Comment on the morphology of the red blood cells.
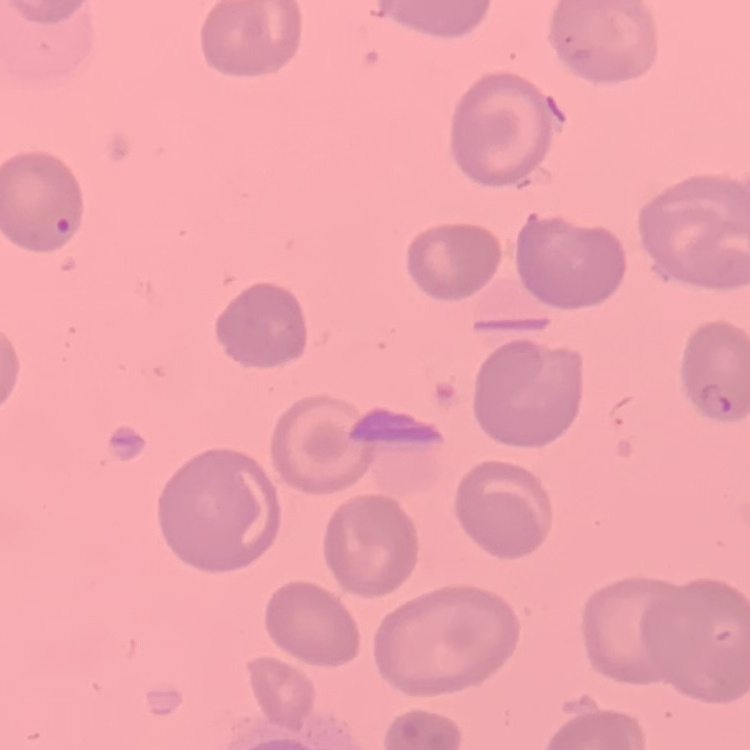
No rouleaux formation.

Summary:
  - Stain: Field's or Giemsa
  - Image type: square crop of a larger photomicrograph
  - Preparation: thin peripheral smear